Name the parasite shown.
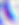
This is Toxoplasma gondii.

Captured at 400x magnification. Photomicrograph.